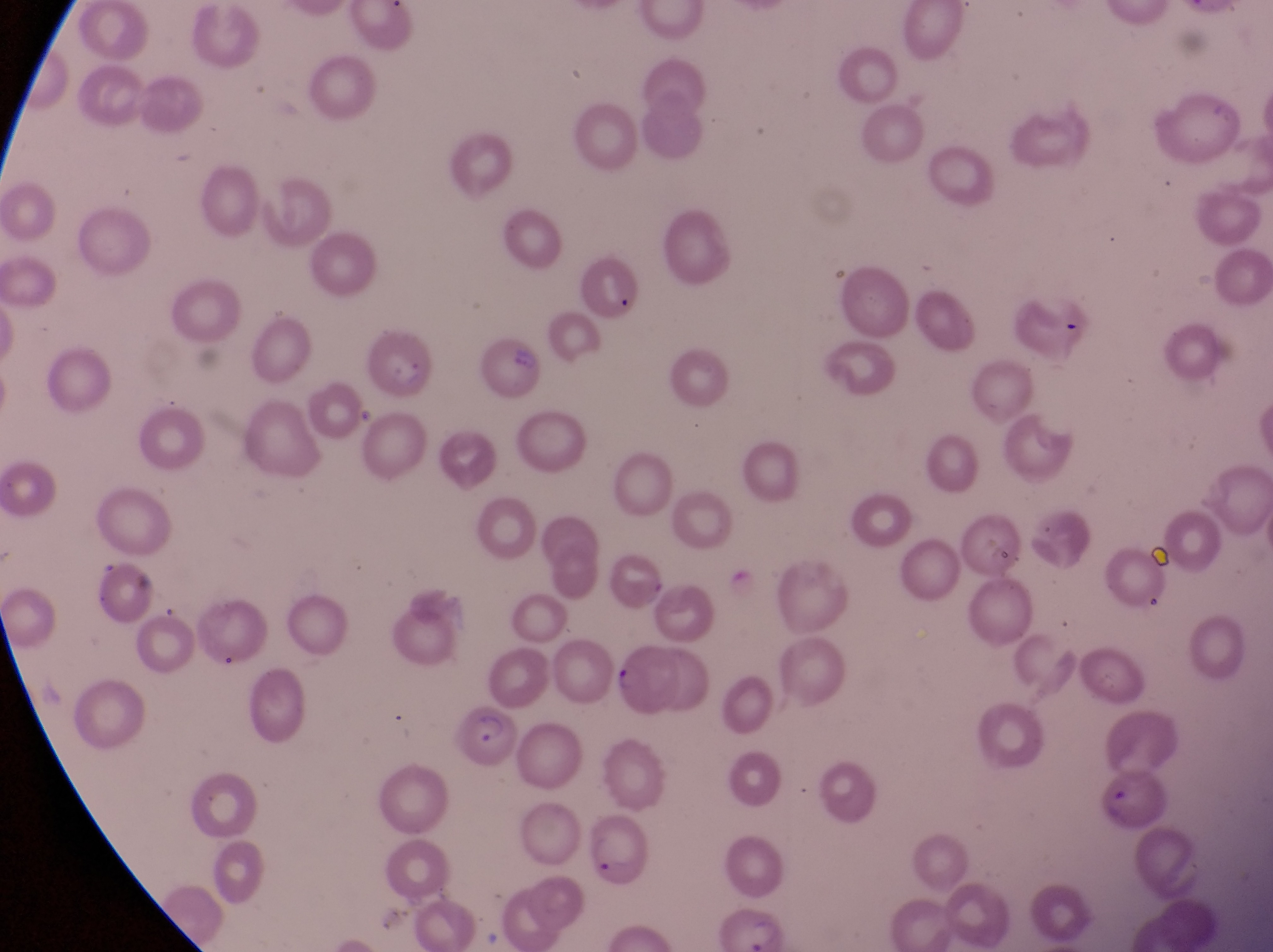
Approximate bounding boxes as [left, top, right, bottom] in pixels.
Summary:
  - Artifact (platelet-like body, stain precipitate, or debris) locations: [499, 339, 536, 371], [384, 360, 431, 393], [130, 569, 157, 602]
  - Parasitised red blood cell locations: [371, 330, 438, 401], [611, 640, 689, 722], [457, 711, 526, 779], [586, 809, 658, 889]
  - Preparation: thin blood smear
  - Field of view: single
  - Magnification: 1000x
  - Image size: 1273×952 pixels
  - Capture: smartphone photograph through the eyepiece of an Olympus CX-23 microscope
  - Country: Uganda